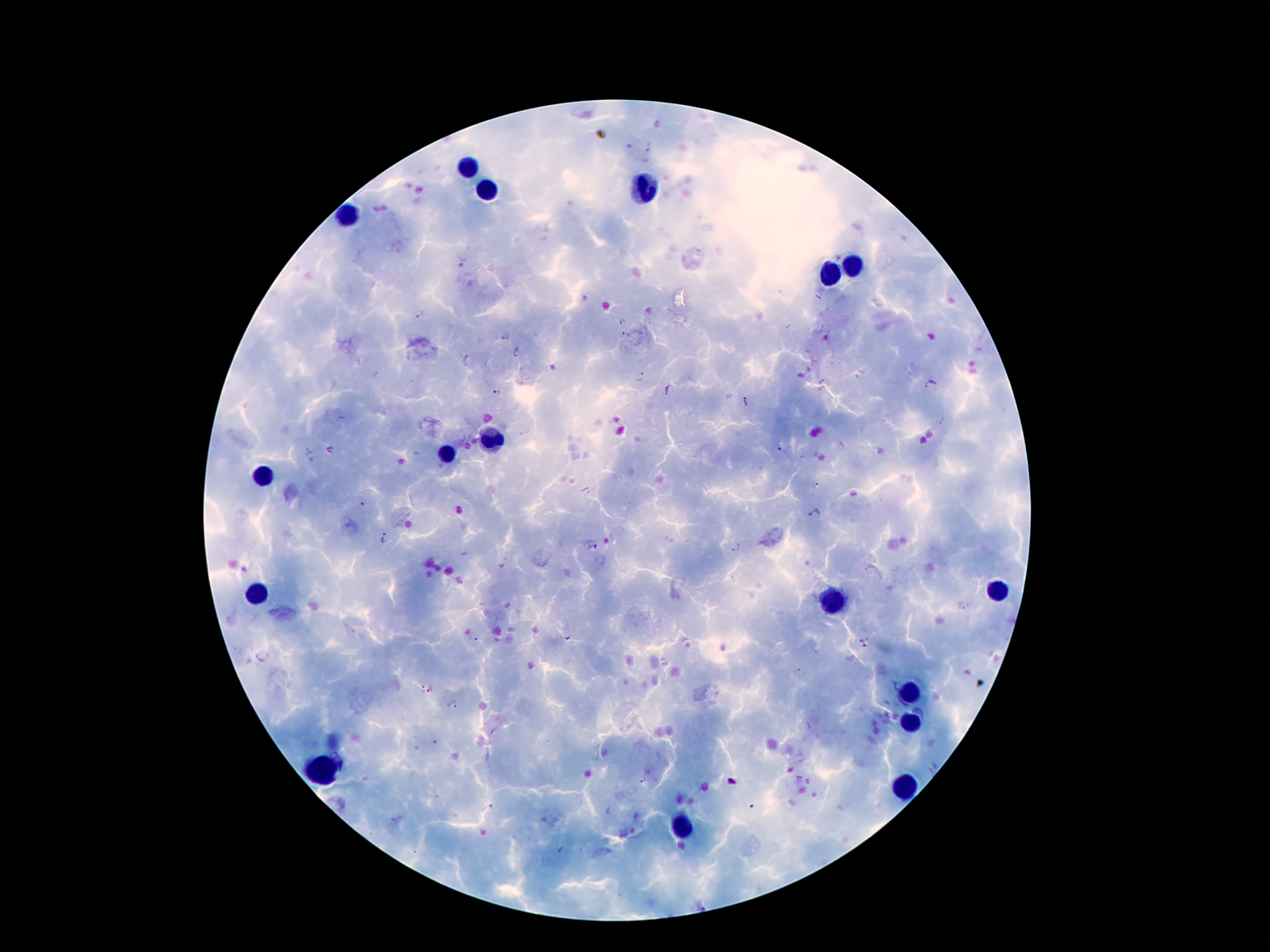

Approximate centers as {x, y} in pixels. Plasmodium parasite locations: {816, 298}, {419, 316}, {622, 321}, {624, 335}, {505, 337}, {518, 352}, {641, 377}, {821, 379}, {930, 386}, {667, 391}, {497, 392}, {746, 402}, {942, 422}, {328, 450}, {781, 452}, {816, 486}, {362, 506}, {460, 511}, {814, 513}, {385, 539}, {737, 547}, {594, 548}, {505, 564}, {474, 638}, {565, 638}, {865, 644}, {799, 672}, {419, 688}, {433, 688}, {453, 706}, {641, 781}, {491, 808}, {608, 811}, {563, 849}. Leukocyte locations: {471, 169}, {651, 188}, {487, 193}, {348, 215}, {850, 261}, {827, 279}, {491, 439}, {446, 458}, {260, 478}, {995, 591}, {258, 595}, {829, 601}, {909, 692}, {911, 720}, {321, 770}, {901, 786}, {682, 828}. Image is 1270×952 pixels. Giemsa-stained preparation. Patient malaria status: positive for Plasmodium falciparum. Smartphone photograph taken through the microscope eyepiece. Thick blood smear. Single field of view. 100x magnification.